Assess this cell for malaria.
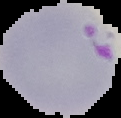
It is parasitized.

image type = segmented cell region with the area outside set to black
image size = 121×118 pixels
preparation = thin blood smear